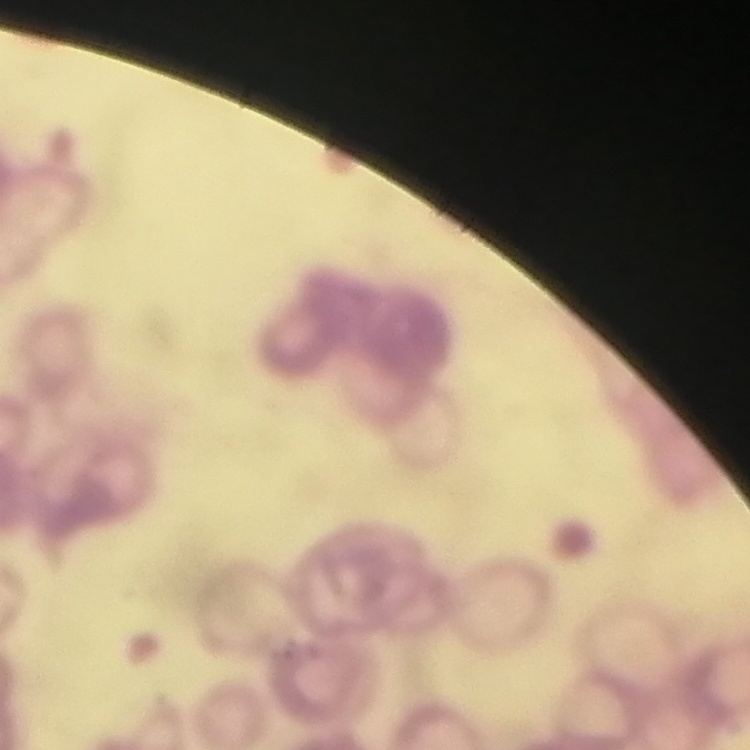
erythrocyte morphology = rouleaux formation
preparation = thin peripheral smear
image type = one tile cut from a larger photomicrograph
stain = Field's or Giemsa